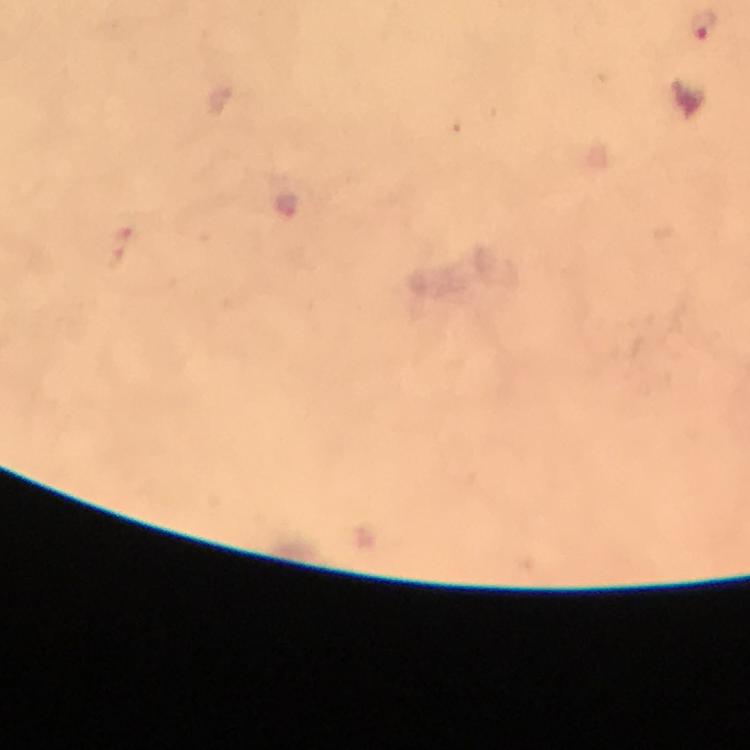
Approximate centers as [x, y] in pixels.
Summary:
  - Plasmodium parasite locations: [704, 23]
  - Stain: Giemsa
  - Cropped from: a single field of view
  - Context: from a diagnostic examination for malaria
  - Immersion oil: used
  - Image size: 750×750 pixels
  - Preparation: thick blood smear
  - Capture: smartphone mounted on the microscope
  - Magnification: 100x